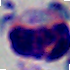

modality = micrograph
magnification = 1000x
identification = white blood cell